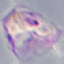

Summary:
  - Result: malaria parasites detected
  - Stain: Giemsa
  - Image type: automatically extracted cell patch, resized to 64 × 64 pixels
  - Preparation: thin smear
  - Capture: smartphone camera at the microscope eyepiece